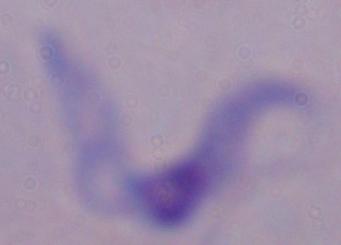
Micrograph. A trypanosome is shown. 1000x magnification.